Classify this cell by malaria status.
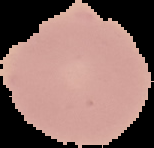
It is uninfected.

image type = segmented cell region on a black background
image size = 154×148 pixels
preparation = thin blood film